Classify this cell by malaria status.
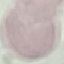
It is uninfected.

Automatically extracted cell patch, resized to 64 × 64 pixels. Acquired by smartphone through the microscope eyepiece. Thin smear of blood. Giemsa stain.